Identify the preparation type.
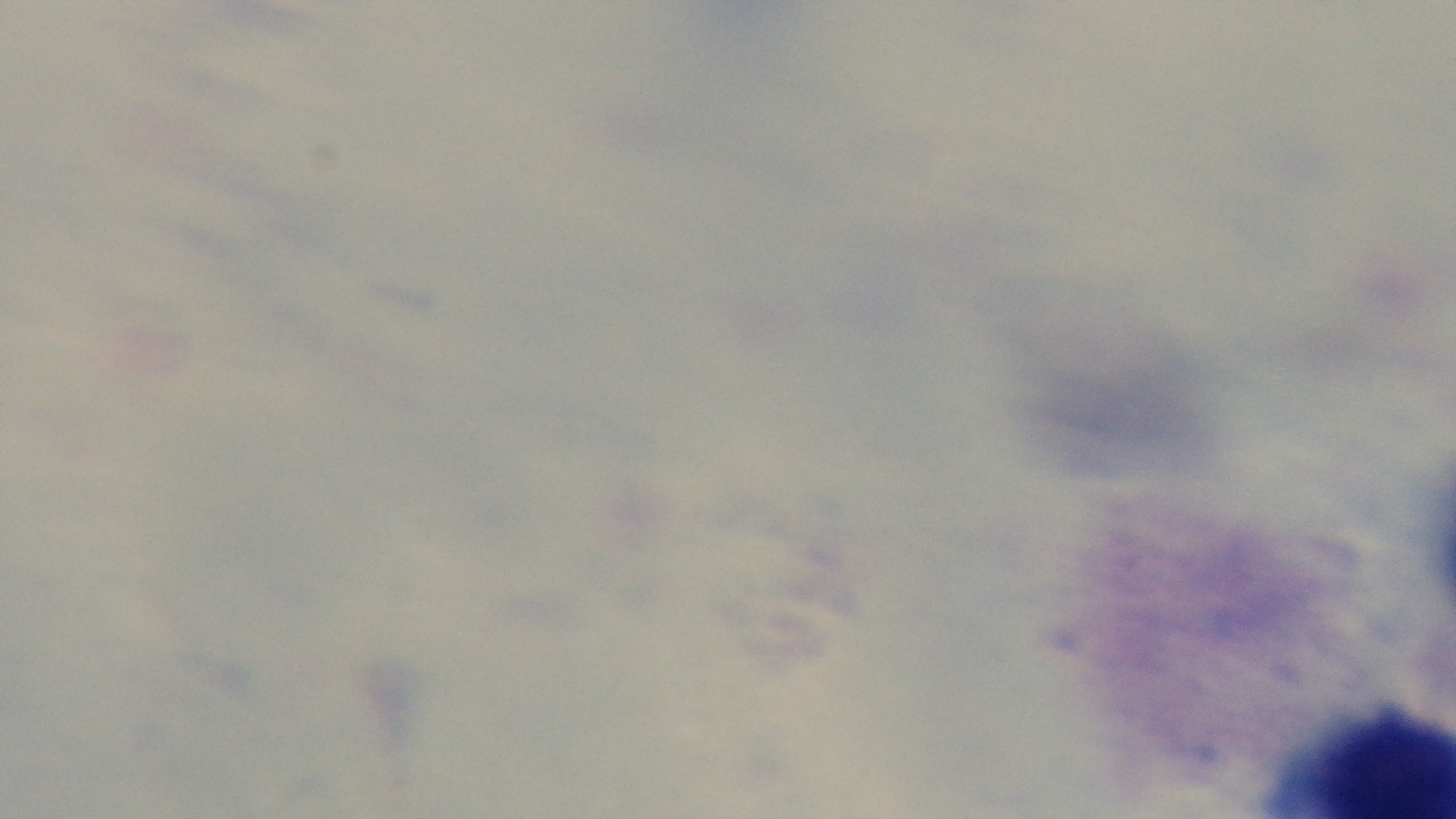
It is a thick blood film.

Summary:
  - Field of view: one from the slide
  - Capture: mounted 4K digital camera
  - Malaria status: uninfected
  - Stain: Giemsa
  - Modality: light microscopy
  - Objective: 100x oil immersion